Locate every Plasmodium parasite.
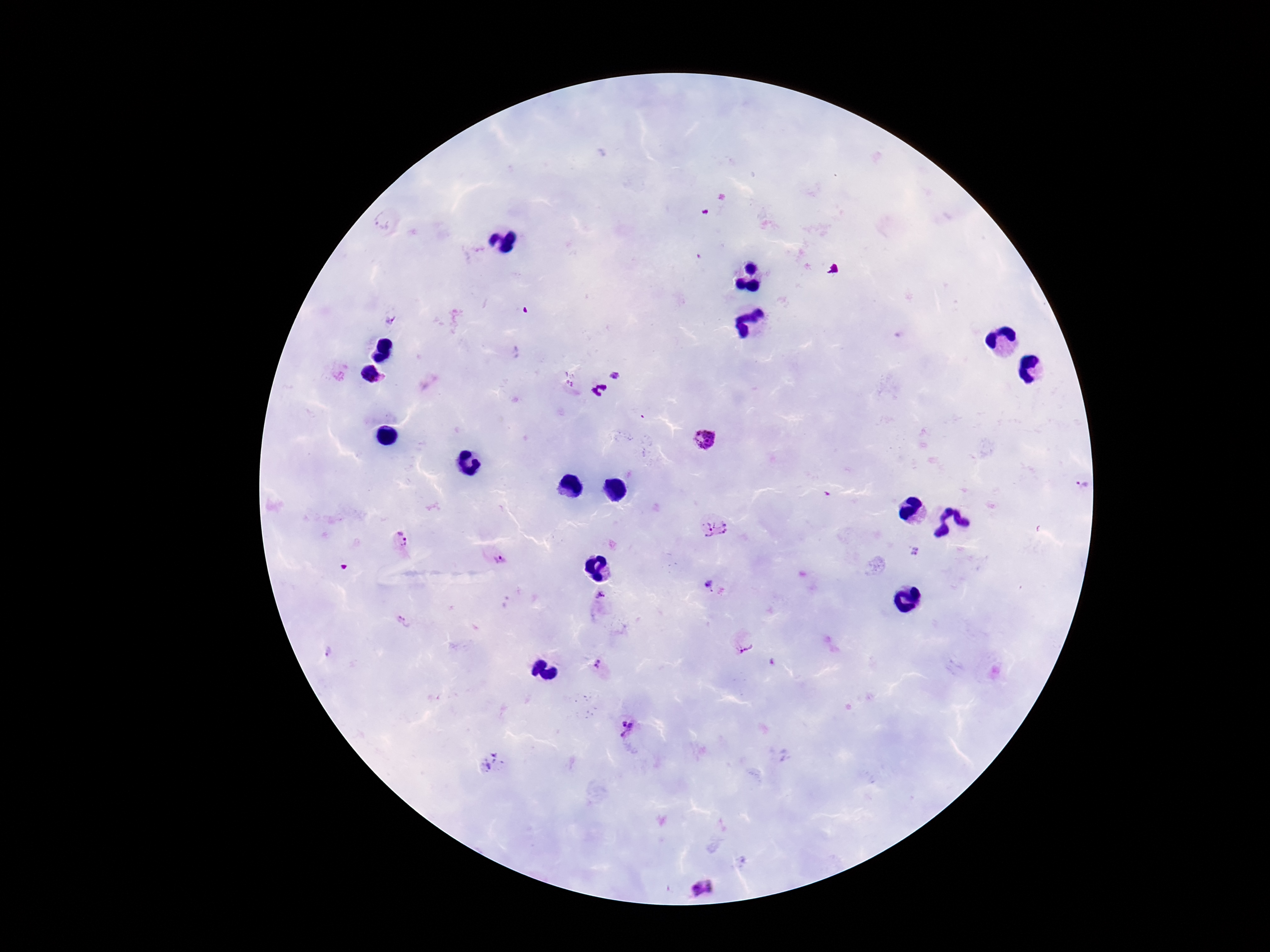

Approximate object centers, in pixels from the top-left corner.
Plasmodium parasites: (x=386, y=219), (x=525, y=310), (x=618, y=374), (x=600, y=391), (x=706, y=437), (x=1078, y=485), (x=713, y=526), (x=400, y=543), (x=915, y=552), (x=496, y=557), (x=708, y=583), (x=600, y=599), (x=743, y=643), (x=598, y=666), (x=626, y=727), (x=492, y=764), (x=701, y=888).

Summary:
  - Magnification: 100x
  - Image size: 1270×952 pixels
  - Stain: Giemsa
  - Capture: smartphone camera through the microscope eyepiece
  - Patient malaria status: infected
  - Field of view: one from this slide
  - Preparation: thick blood film